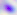

Summary:
  - Magnification: 400x
  - Modality: micrograph
  - Identification: Toxoplasma gondii